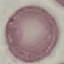
Result: negative for malaria parasites. Automatically extracted cell patch, resized to 64 × 64 pixels. Giemsa-stained preparation. Photographed with a smartphone camera at the microscope eyepiece. Thin smear of blood.